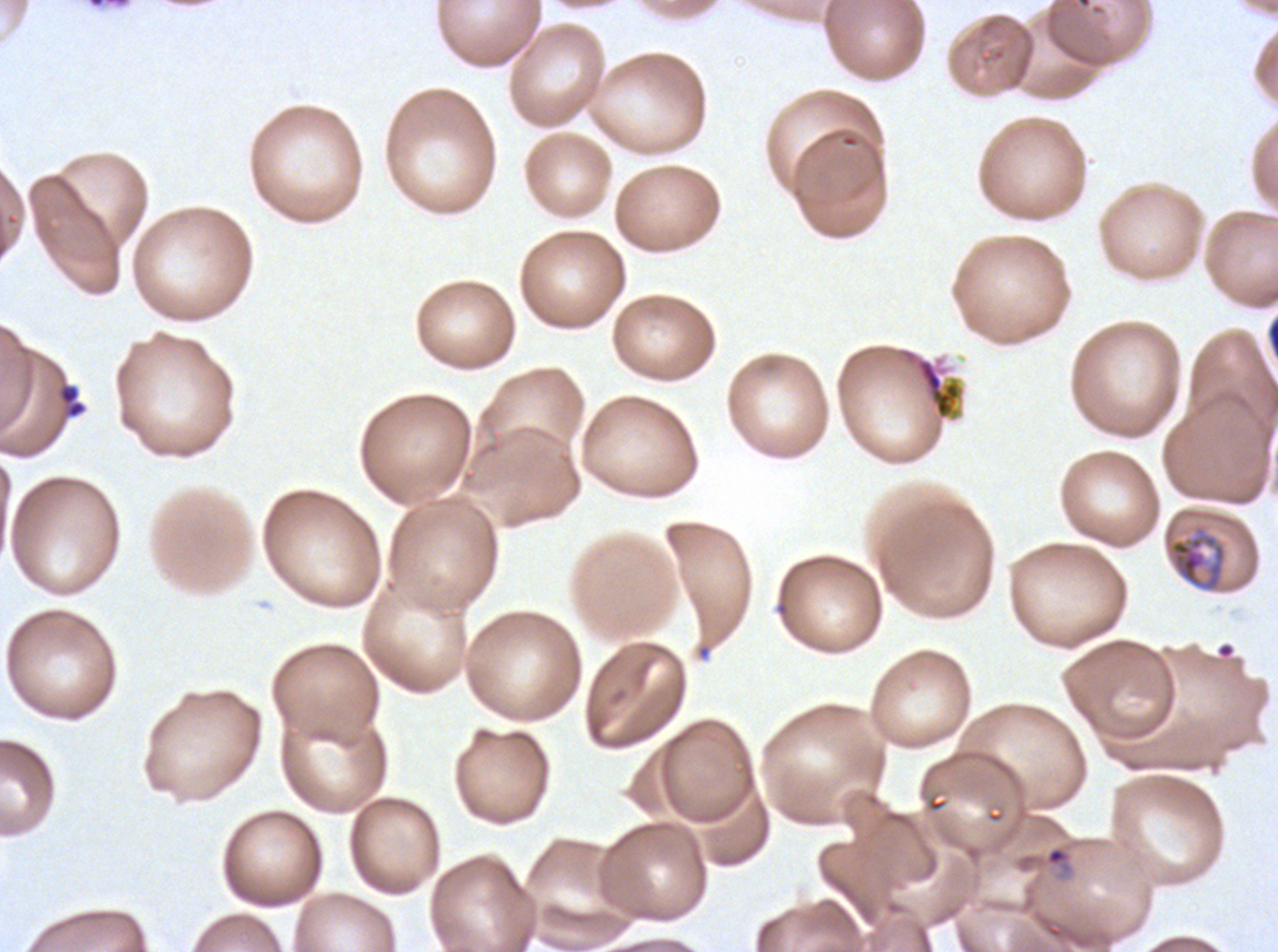
Approximate bounding rectangles given as corner coordinates in pixels from the top-left. Mid trophozoite locations: (x1=1168, y1=532, x2=1227, y2=592). Ring locations: (x1=56, y1=383, x2=88, y2=420), (x1=1044, y1=845, x2=1073, y2=874). Debris locations: (x1=915, y1=358, x2=961, y2=419). Image is 1278×952 pixels. Life-cycle stages observed: ring, mid trophozoite. Thin blood film. P. falciparum cultured ex vivo for 24 to 48 hours, from a patient in The Gambia. Giemsa-stained preparation. One sub-image of a larger composite.